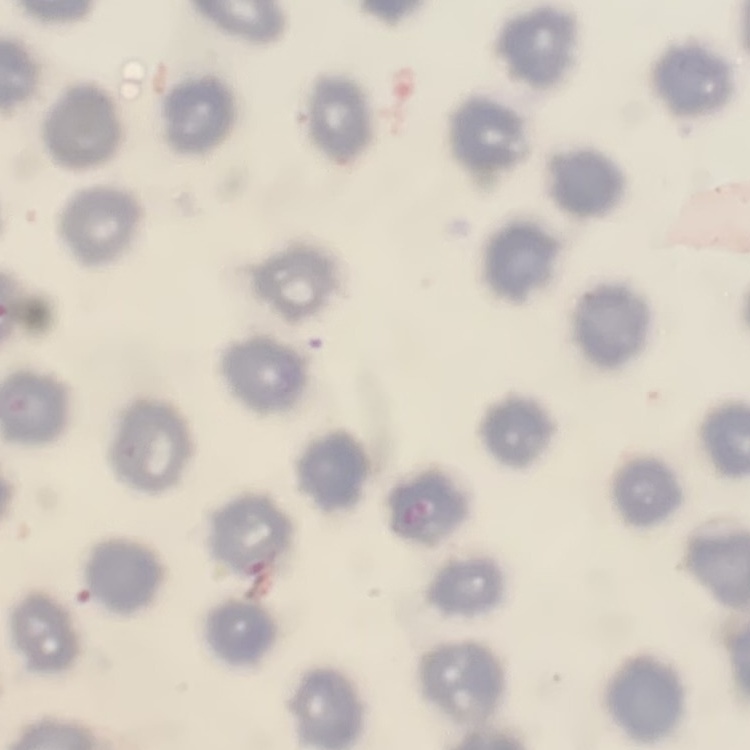

Summary:
  - Red blood cell morphology: no rouleaux formation
  - Preparation: thin peripheral smear
  - Image type: square crop of a larger photomicrograph
  - Stain: Field's or Giemsa